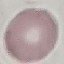

malaria status = uninfected
capture = smartphone camera at the microscope eyepiece
stain = Giemsa
preparation = thin blood film
image type = cell patch, automatically extracted from a larger field of view and resized to 64 × 64 pixels